Locate every blood parasite and identify its species.
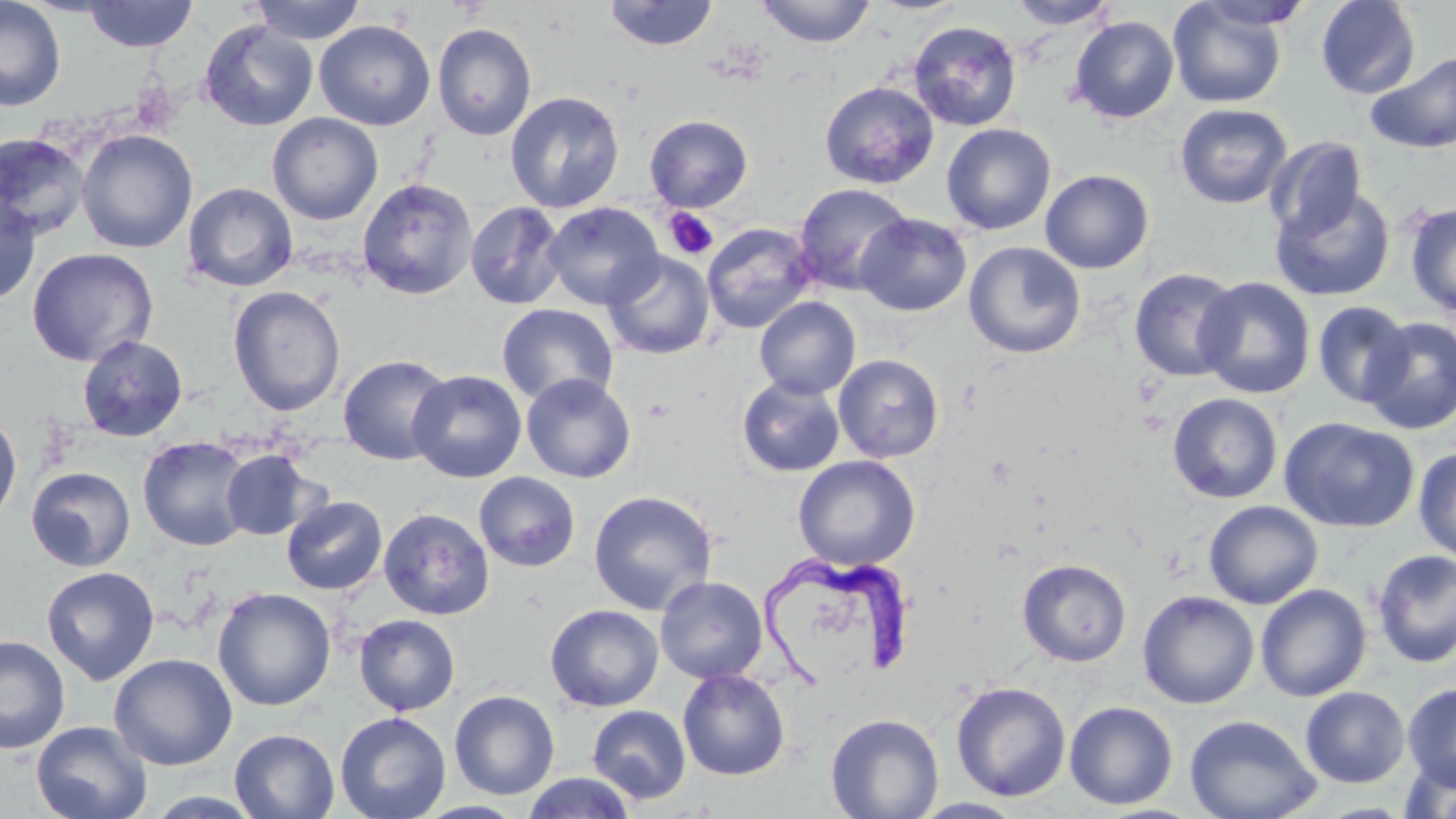

Approximate bounding boxes as (x1, y1, x2, y2) in pixels.
Trypanosoma brucei: (761, 553, 916, 690).
No Plasmodium falciparum, Plasmodium ovale, Plasmodium malariae, Plasmodium vivax, or Babesia divergens observed.

Platelet locations: (663, 207, 719, 260). Uninfected red blood cell locations: (0, 0, 66, 111), (249, 0, 366, 44), (756, 0, 876, 47), (1006, 0, 1118, 29), (1167, 0, 1288, 109), (1315, 0, 1420, 99), (82, 1, 198, 52), (603, 1, 718, 51), (1069, 16, 1179, 124), (199, 20, 318, 131), (314, 20, 436, 130), (908, 20, 1022, 132), (432, 23, 537, 141), (1365, 51, 1456, 153), (819, 81, 939, 189), (505, 91, 625, 214), (1174, 103, 1293, 209), (267, 113, 383, 225), (644, 114, 754, 213), (941, 124, 1057, 234), (76, 129, 198, 253), (0, 132, 91, 240), (1264, 137, 1367, 242), (1040, 169, 1154, 274), (357, 178, 477, 299), (183, 183, 298, 292), (793, 183, 914, 295), (1270, 186, 1395, 302), (0, 192, 42, 308), (465, 201, 567, 310), (542, 202, 664, 310), (1405, 202, 1456, 319), (856, 213, 971, 317), (701, 223, 817, 334), (963, 241, 1085, 358), (26, 247, 159, 367), (603, 250, 714, 360), (1129, 267, 1243, 382), (1194, 277, 1315, 399), (227, 286, 346, 417), (754, 297, 861, 400), (1312, 301, 1414, 408), (496, 304, 618, 406), (1360, 317, 1456, 434), (77, 335, 189, 442), (337, 354, 454, 465), (834, 354, 944, 462), (408, 370, 527, 483), (521, 373, 636, 483), (737, 376, 845, 477), (1167, 392, 1283, 503), (0, 410, 22, 526), (1279, 417, 1420, 533), (137, 435, 255, 552), (1413, 447, 1456, 562), (221, 449, 319, 541), (793, 455, 920, 571), (26, 466, 137, 572), (474, 472, 580, 572), (587, 490, 718, 615), (281, 495, 388, 595), (1203, 500, 1323, 609), (379, 508, 495, 620), (1372, 549, 1456, 668), (1017, 558, 1132, 667), (41, 566, 160, 686), (655, 576, 767, 683), (1255, 583, 1372, 702), (213, 586, 336, 711), (1137, 590, 1259, 709), (545, 604, 663, 712), (353, 614, 460, 716), (0, 634, 70, 753), (109, 653, 237, 770), (677, 669, 790, 781), (951, 680, 1071, 802), (1402, 682, 1456, 792), (1300, 686, 1410, 788), (449, 690, 560, 800), (1064, 701, 1178, 810), (587, 705, 691, 804), (335, 712, 451, 819), (825, 713, 944, 819), (1184, 714, 1321, 819), (31, 720, 153, 819), (229, 729, 340, 818), (1400, 755, 1456, 819), (522, 772, 638, 818), (911, 797, 1027, 818). Slide-level diagnosis: Trypanosoma brucei. Thin blood film. May-Grünwald-Giemsa stain. Captured at 1000x magnification. Image is 1456×819 pixels. Optical microscopy. One field of a larger specimen.